Assess this cell for malaria.
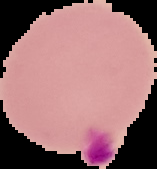
It is parasitized.

From a thin blood smear. Image is 157×169 pixels. The area outside the segmented cell region is set to black.